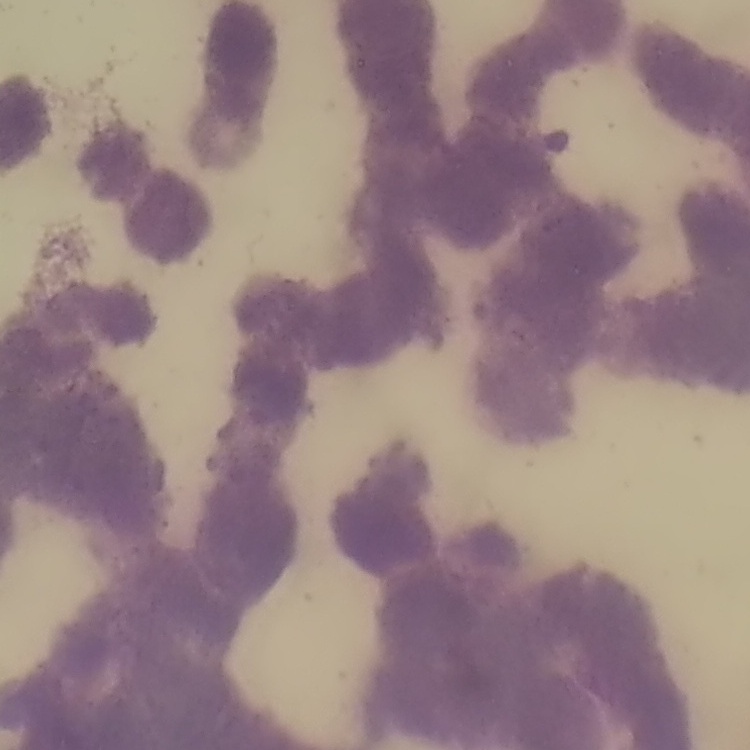

Summary:
  - Erythrocyte morphology: rouleaux formation
  - Image type: one tile cut from a larger photomicrograph
  - Preparation: thin peripheral smear
  - Stain: Field's or Giemsa